Describe the morphology of the erythrocytes.
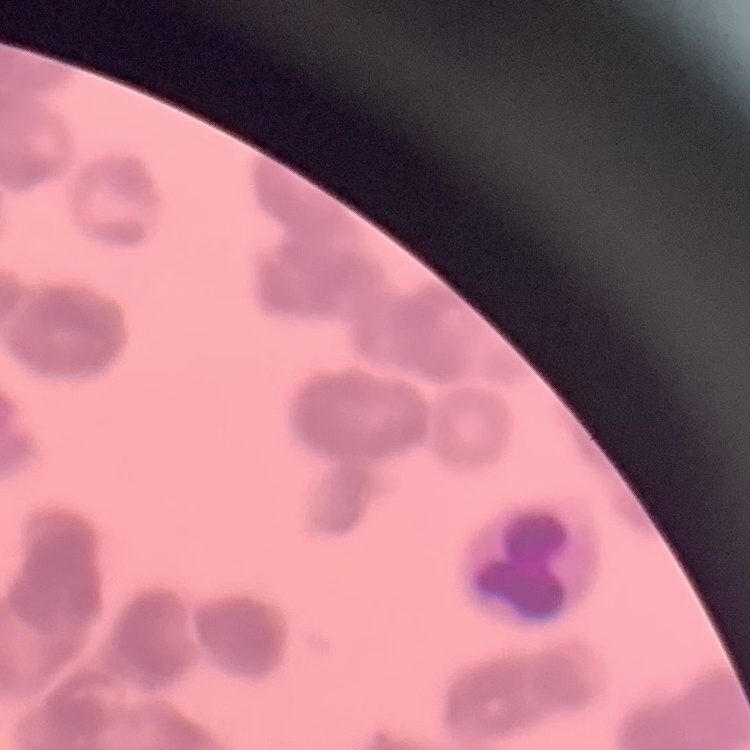
Rouleaux formation.

Summary:
  - Image type: square crop of a larger photomicrograph
  - Stain: Field's or Giemsa
  - Preparation: thin peripheral smear